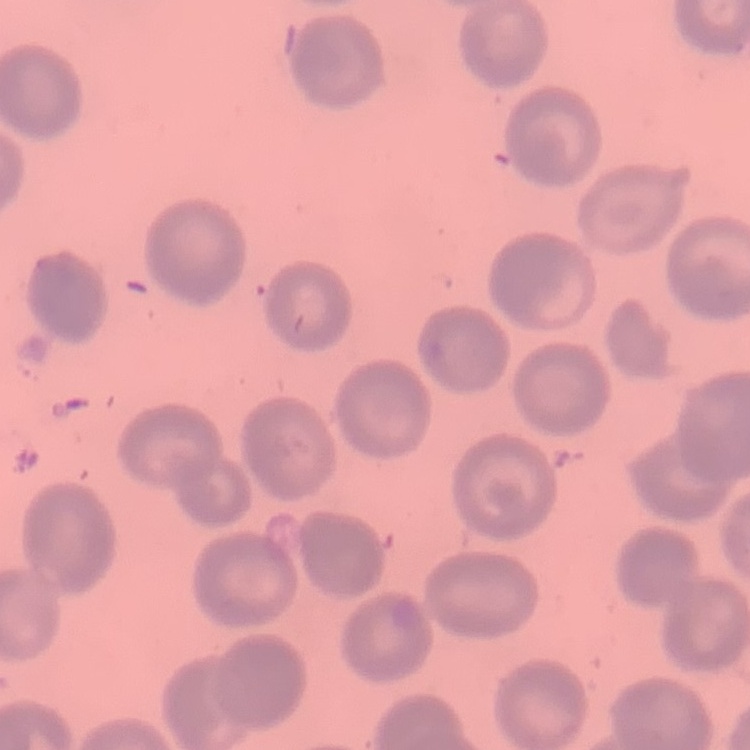
The erythrocytes exhibit no rouleaux formation. Thin blood smear. Square crop of a larger photomicrograph. Stained with either Field's or Giemsa.